Assess this cell for malaria.
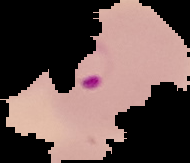

It is parasitized.

Summary:
  - Image type: cell region segmented out of the field of view; surrounding area masked to black
  - Preparation: thin blood smear
  - Image size: 190×163 pixels